Assess this cell for malaria.
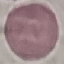
It is uninfected.

Summary:
  - Capture: smartphone through the microscope eyepiece
  - Image type: automatically extracted cell patch, resized to 64 × 64 pixels
  - Preparation: thin blood film
  - Stain: Giemsa